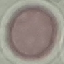

Summary:
  - Malaria status: uninfected
  - Image type: cell patch, automatically extracted from a larger field of view and resized to 64 × 64 pixels
  - Capture: smartphone through the microscope eyepiece
  - Preparation: thin smear
  - Stain: Giemsa